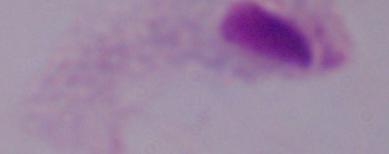
modality = photomicrograph
magnification = 1000x
identification = trichomonad